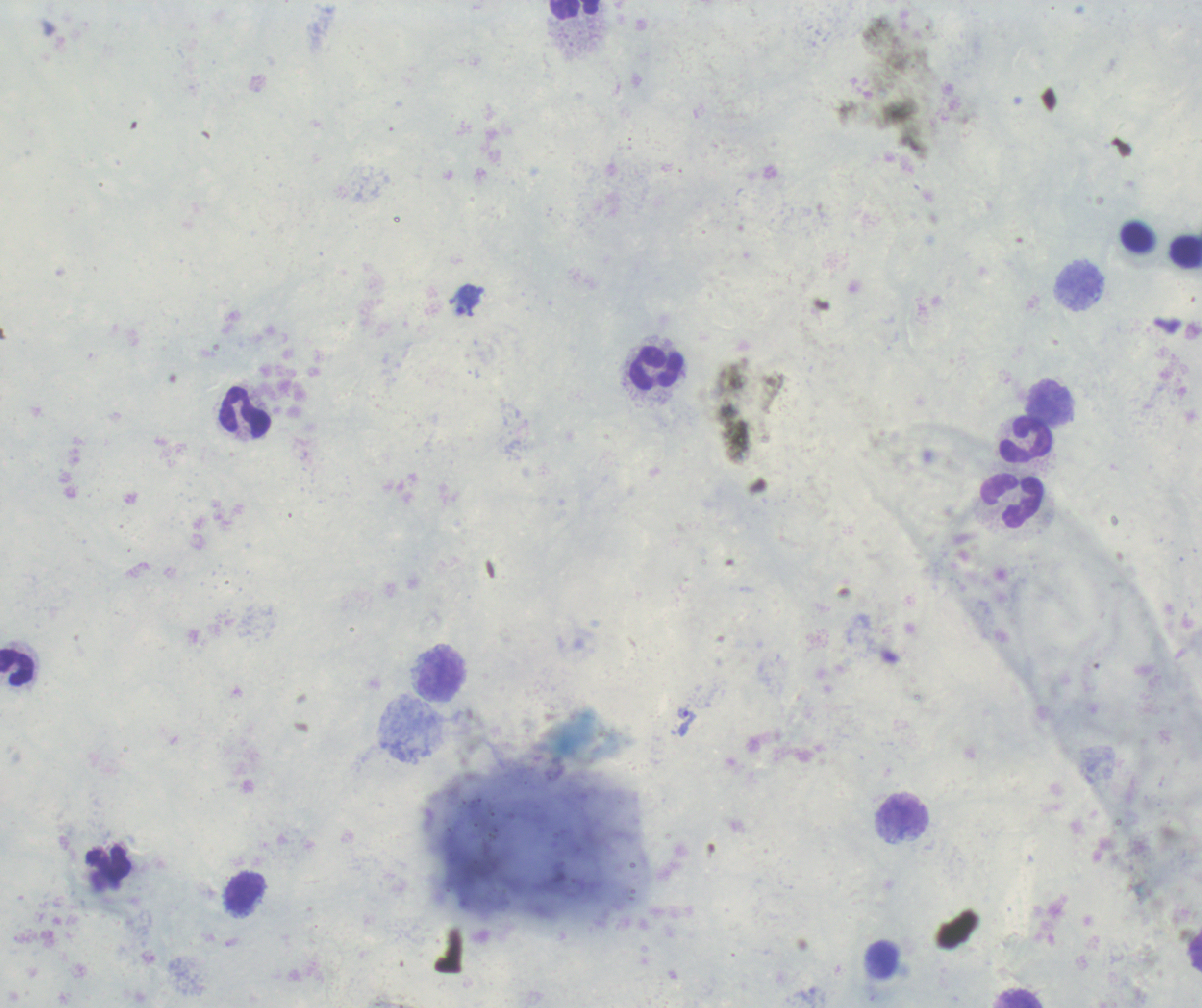

Approximate centers as {x, y} in pixels. Leukocyte locations: {576, 10}, {1185, 250}, {1078, 286}, {657, 368}, {1049, 405}, {245, 412}, {1026, 441}, {1012, 502}, {17, 667}, {440, 675}, {903, 816}, {108, 864}, {245, 894}, {1019, 999}. Trophozoite locations: {466, 301}, {685, 721}. Romanowsky-stained preparation. Image is 1202×1008 pixels. Coloration quality: good. Previously used in an actual diagnosis. 100x magnification. Thick smear of blood. One field from this slide. Result: positive for malaria parasites. Background quality: poor.